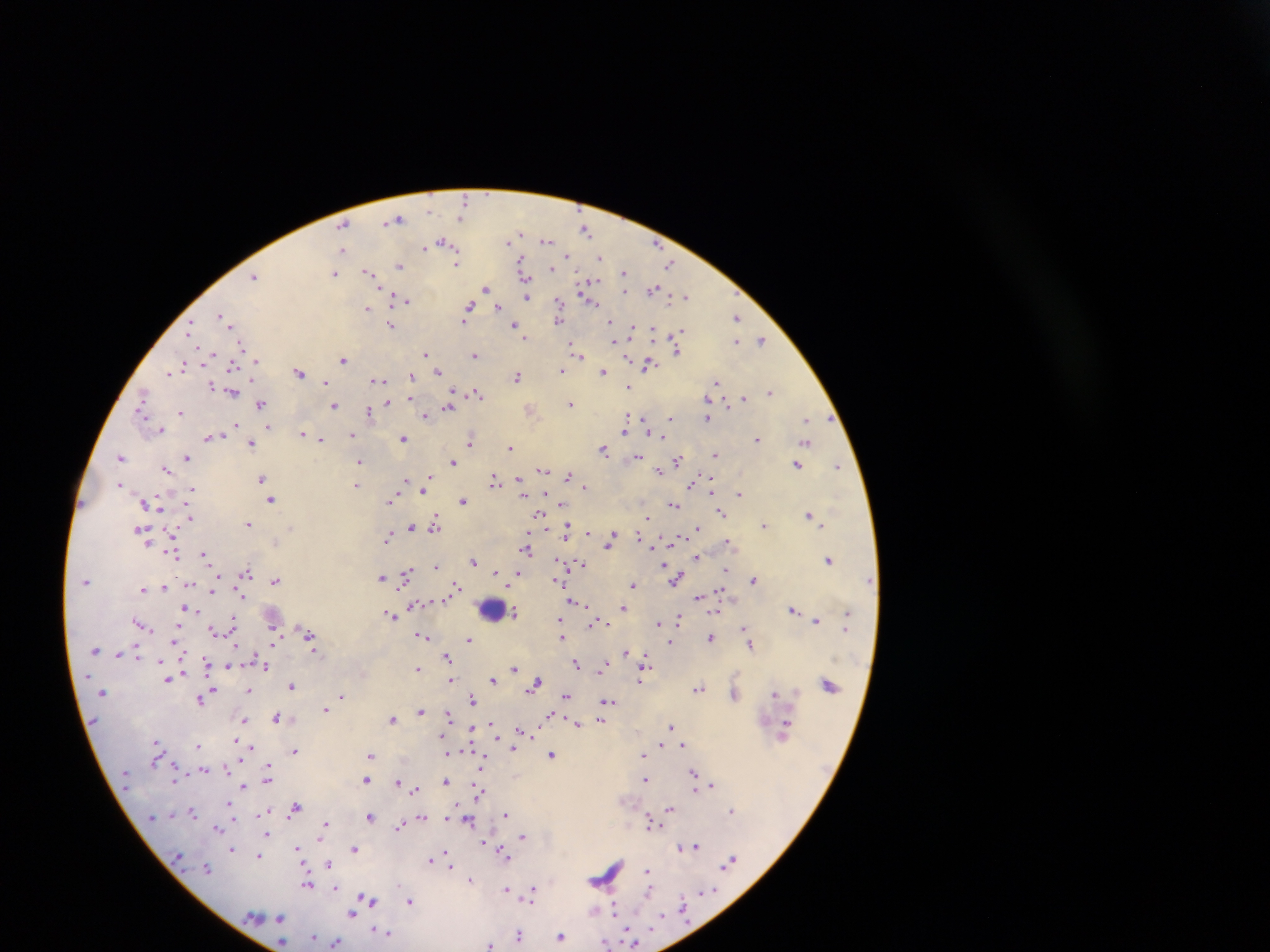
Approximate centers as {x, y} in pixels.
Summary:
  - Malaria parasite locations: {465, 201}, {429, 210}, {460, 217}, {397, 219}, {343, 225}, {586, 230}, {521, 232}, {546, 241}, {442, 242}, {509, 242}, {423, 247}, {342, 249}, {568, 257}, {600, 257}, {522, 261}, {456, 263}, {399, 265}, {670, 265}, {552, 269}, {368, 272}, {335, 273}, {624, 273}, {254, 276}, {524, 278}, {590, 284}, {485, 288}, {653, 289}, {584, 291}, {625, 291}, {685, 296}, {526, 297}, {406, 300}, {558, 303}, {593, 303}, {469, 307}, {499, 307}, {367, 308}, {221, 315}, {737, 317}, {463, 320}, {558, 321}, {227, 323}, {391, 325}, {515, 325}, {612, 325}, {191, 327}, {633, 329}, {652, 330}, {679, 334}, {525, 337}, {615, 339}, {761, 340}, {737, 341}, {241, 345}, {572, 345}, {677, 349}, {209, 354}, {426, 354}, {577, 354}, {475, 355}, {255, 360}, {343, 360}, {182, 365}, {648, 365}, {232, 367}, {562, 370}, {171, 371}, {299, 371}, {438, 371}, {603, 371}, {412, 376}, {517, 377}, {376, 380}, {325, 382}, {715, 383}, {212, 386}, {629, 386}, {770, 391}, {233, 393}, {477, 393}, {453, 394}, {143, 396}, {744, 398}, {410, 399}, {387, 403}, {570, 403}, {261, 404}, {334, 406}, {448, 407}, {369, 411}, {181, 412}, {141, 413}, {426, 415}, {642, 418}, {671, 418}, {707, 418}, {808, 420}, {235, 424}, {267, 426}, {647, 427}, {160, 429}, {624, 430}, {303, 434}, {351, 435}, {663, 436}, {210, 438}, {404, 438}, {320, 439}, {757, 439}, {471, 440}, {806, 443}, {251, 445}, {510, 447}, {604, 449}, {715, 454}, {121, 457}, {639, 457}, {188, 458}, {677, 460}, {453, 462}, {359, 463}, {797, 465}, {838, 466}, {166, 469}, {543, 470}, {659, 471}, {569, 476}, {261, 478}, {407, 480}, {494, 480}, {519, 480}, {120, 484}, {691, 484}, {357, 485}, {521, 485}, {426, 486}, {584, 487}, {191, 489}, {424, 491}, {711, 491}, {523, 493}, {739, 494}, {392, 498}, {271, 499}, {462, 501}, {673, 505}, {722, 513}, {540, 514}, {809, 514}, {190, 517}, {646, 518}, {248, 524}, {763, 525}, {435, 526}, {411, 527}, {698, 528}, {141, 530}, {567, 531}, {588, 534}, {615, 536}, {639, 536}, {389, 537}, {611, 539}, {276, 542}, {729, 542}, {526, 549}, {204, 554}, {174, 555}, {697, 557}, {829, 560}, {473, 561}, {581, 564}, {437, 565}, {725, 570}, {495, 572}, {246, 573}, {407, 574}, {517, 576}, {382, 577}, {676, 579}, {754, 579}, {559, 580}, {276, 581}, {633, 585}, {164, 587}, {455, 587}, {142, 589}, {213, 589}, {719, 593}, {698, 597}, {574, 601}, {624, 607}, {188, 609}, {793, 609}, {514, 614}, {391, 616}, {678, 619}, {233, 621}, {816, 621}, {139, 622}, {596, 622}, {659, 623}, {561, 625}, {744, 629}, {214, 631}, {308, 635}, {422, 635}, {562, 635}, {175, 639}, {710, 639}, {469, 640}, {670, 642}, {750, 646}, {626, 652}, {447, 656}, {645, 660}, {263, 663}, {577, 664}, {603, 665}, {228, 666}, {418, 668}, {514, 668}, {168, 679}, {492, 679}, {451, 680}, {640, 680}, {535, 683}, {292, 686}, {699, 689}, {250, 690}, {775, 692}, {341, 696}, {566, 696}, {733, 696}, {201, 699}, {472, 700}, {607, 701}, {325, 709}, {421, 711}, {448, 715}, {277, 718}, {391, 719}, {601, 720}, {243, 721}, {578, 724}, {671, 726}, {492, 727}, {785, 727}, {521, 731}, {471, 732}, {157, 742}, {662, 745}, {682, 745}, {198, 746}, {512, 748}, {295, 750}, {371, 755}, {552, 755}, {643, 756}, {204, 769}, {694, 773}, {268, 776}, {365, 780}, {645, 780}, {445, 781}, {397, 782}, {243, 786}, {712, 786}, {702, 787}, {415, 789}, {694, 789}, {478, 793}, {295, 807}, {669, 809}, {731, 810}, {192, 811}, {264, 815}, {506, 815}, {371, 816}, {421, 817}, {469, 821}, {650, 821}, {325, 826}, {399, 826}, {218, 828}, {267, 833}, {523, 836}, {485, 843}, {696, 846}, {680, 847}, {298, 849}, {355, 849}, {232, 850}, {504, 853}, {259, 856}, {430, 860}, {448, 860}, {729, 862}, {328, 863}, {206, 868}, {648, 870}, {470, 879}, {307, 884}, {336, 888}, {506, 890}, {532, 890}, {648, 891}, {367, 899}, {410, 901}, {616, 910}, {594, 911}, {353, 913}, {280, 918}, {387, 933}, {519, 935}, {561, 937}, {313, 938}, {336, 942}, {282, 943}, {606, 944}, {490, 945}
  - Leukocyte locations: {493, 610}
  - Image size: 1270×952 pixels
  - Preparation: thick blood film
  - Capture: mobile-phone photograph through a microscope
  - Country: Ghana
  - Field of view: single